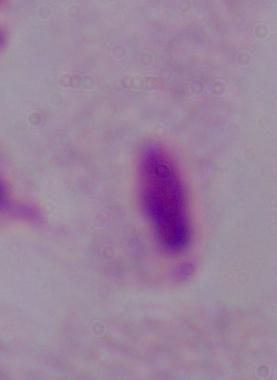
Summary:
  - Magnification: 1000x
  - Identification: trichomonad
  - Modality: photomicrograph